Classify this cell by malaria status.
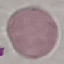

Uninfected.

Summary:
  - Capture: smartphone camera at the microscope eyepiece
  - Stain: Giemsa
  - Preparation: thin blood film
  - Image type: cell patch, automatically extracted from a larger field of view and resized to 64 × 64 pixels